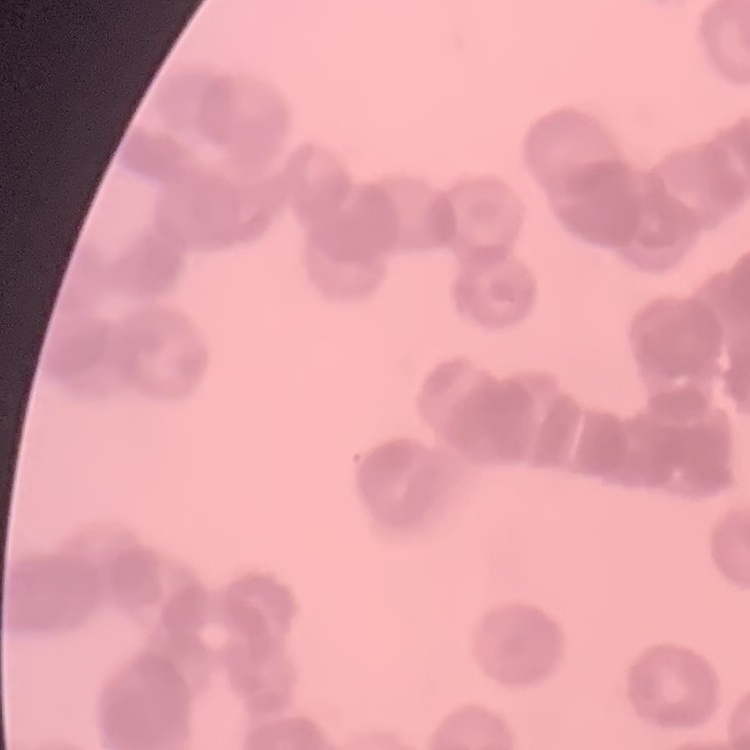
The red blood cells show rouleaux formation. Field's or Giemsa stain. Square crop of a larger photomicrograph. Thin peripheral smear.